Locate every Babesia divergens-infected red blood cell.
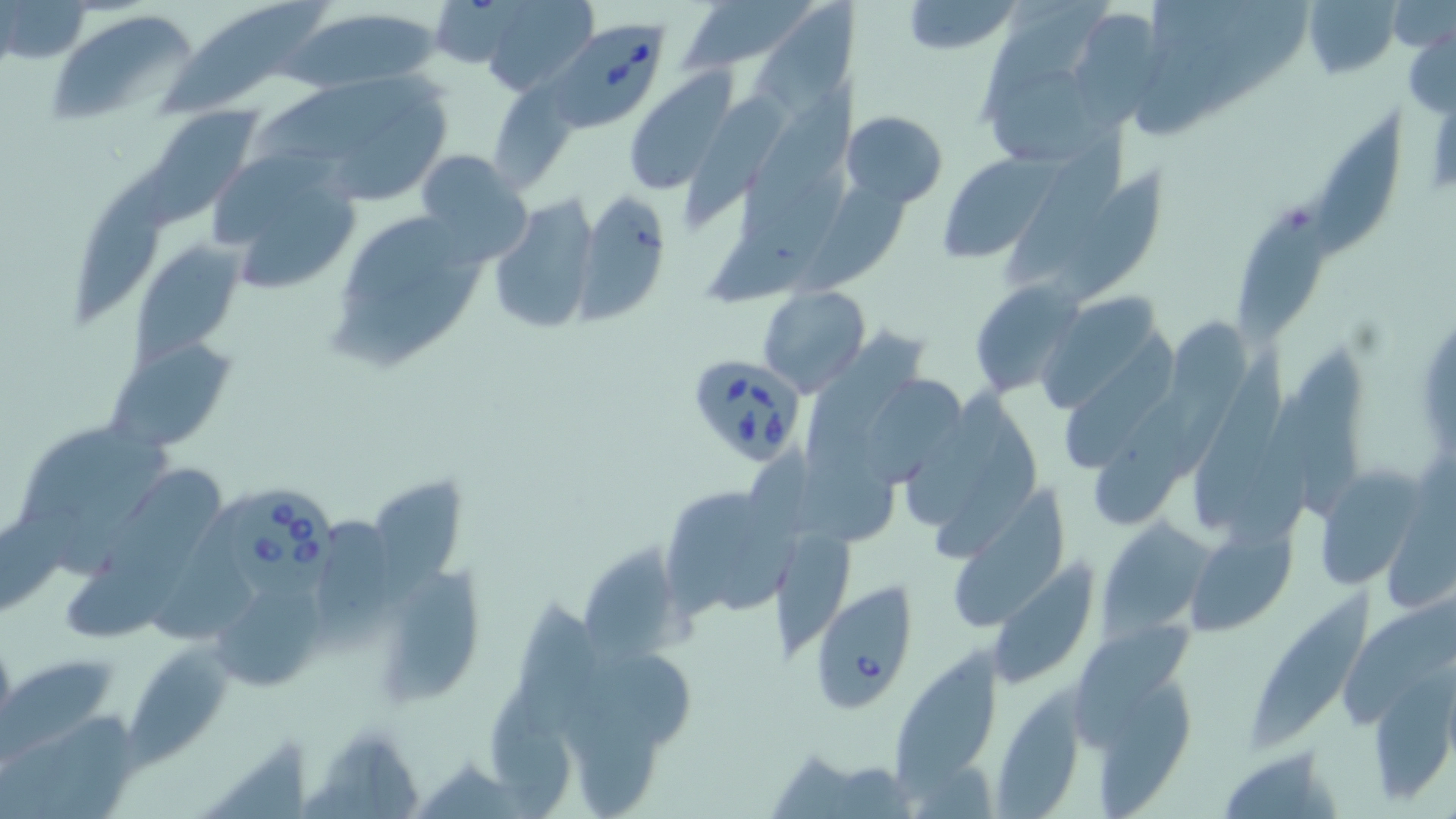
Approximate bounding boxes as [x1, y1, x2, y2] in pixels.
Babesia divergens-infected red blood cells: [555, 21, 667, 132], [685, 352, 809, 467], [224, 481, 345, 603], [811, 579, 920, 708].

Summary:
  - Uninfected red blood cell locations: [163, 0, 332, 111], [425, 0, 531, 70], [677, 0, 812, 77], [900, 0, 1021, 54], [980, 0, 1110, 122], [1302, 0, 1409, 73], [2, 1, 91, 70], [475, 1, 598, 94], [752, 1, 861, 117], [1199, 1, 1307, 115], [1387, 2, 1453, 52], [285, 5, 445, 95], [45, 10, 201, 124], [1404, 27, 1455, 113], [252, 64, 446, 157], [623, 68, 734, 194], [993, 70, 1120, 164], [740, 80, 865, 238], [491, 82, 577, 188], [686, 92, 799, 226], [322, 96, 451, 209], [1314, 105, 1403, 263], [149, 107, 262, 215], [843, 110, 947, 205], [1005, 125, 1131, 285], [418, 149, 529, 259], [213, 151, 338, 245], [938, 155, 1055, 262], [1049, 162, 1180, 312], [72, 163, 172, 333], [704, 164, 845, 311], [794, 169, 916, 302], [1240, 186, 1337, 346], [578, 191, 671, 319], [240, 194, 356, 293], [487, 195, 600, 336], [344, 212, 461, 306], [132, 240, 247, 363], [333, 247, 483, 374], [968, 279, 1084, 400], [1043, 283, 1163, 412], [759, 285, 870, 396], [1166, 319, 1250, 473], [1062, 322, 1184, 473], [816, 329, 932, 445], [104, 337, 236, 455], [1192, 340, 1290, 528], [1287, 348, 1369, 523], [863, 370, 973, 490], [807, 387, 897, 544], [905, 387, 1010, 531], [1093, 394, 1187, 524], [1229, 394, 1309, 555], [934, 415, 1047, 562], [20, 424, 170, 526], [1313, 465, 1425, 590], [70, 468, 231, 640], [373, 482, 469, 605], [660, 484, 798, 619], [955, 485, 1074, 632], [1385, 493, 1456, 611], [149, 498, 259, 639], [0, 504, 89, 621], [317, 517, 393, 648], [1096, 521, 1210, 636], [1185, 527, 1295, 635], [772, 529, 859, 661], [583, 545, 701, 661], [375, 562, 490, 706], [989, 562, 1100, 686], [1258, 577, 1369, 743], [220, 587, 322, 691], [513, 589, 610, 745], [1344, 599, 1456, 729], [1080, 620, 1198, 743], [126, 634, 237, 776], [901, 643, 1004, 801], [0, 658, 112, 769], [1369, 676, 1455, 805], [1098, 677, 1200, 819], [494, 687, 570, 819], [993, 691, 1084, 819], [577, 694, 665, 818], [44, 704, 138, 819], [210, 734, 315, 819], [323, 735, 428, 819], [1215, 746, 1345, 818]
  - Slide-level diagnosis: Babesia divergens
  - Field of view: one of a larger specimen
  - Magnification: 1000x
  - Image size: 1456×819 pixels
  - Stain: May-Grünwald-Giemsa
  - Preparation: thin blood film
  - Modality: optical microscopy